Assess this cell for malaria.
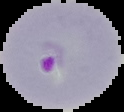

Parasitized.

image size = 124×112 pixels
preparation = thin blood smear
image type = segmented cell region with the area outside set to black